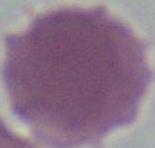

Summary:
  - Modality: photomicrograph
  - Identification: red blood cell
  - Magnification: 1000x